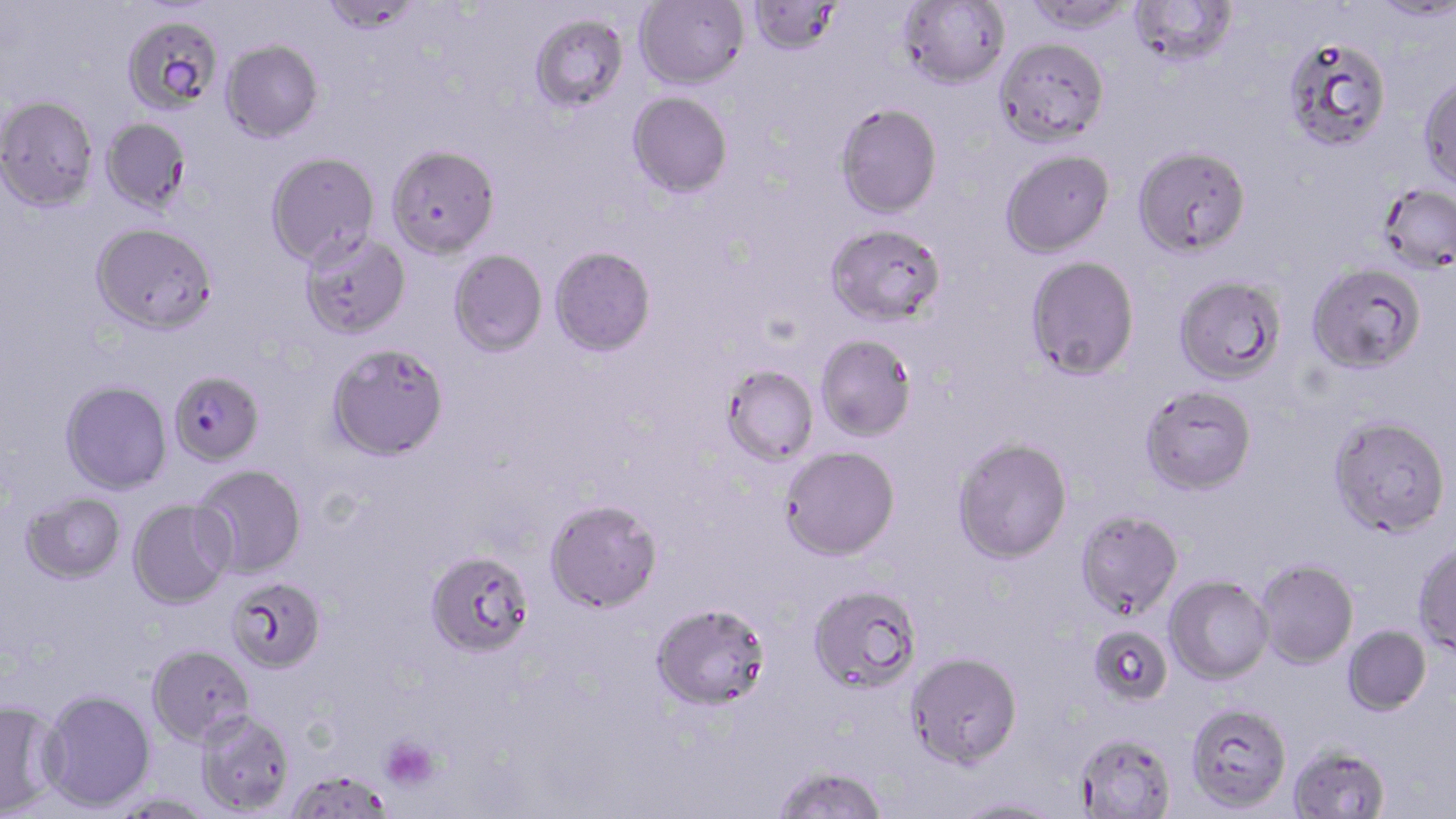
Approximate bounding boxes as (x1,y1)-(x2,y2) corner pairs in pixels. Platelet locations: (379,736)-(441,792). Plasmodium falciparum-infected red blood cell locations: (169,370)-(264,466). Uninfected red blood cell locations: (634,0)-(748,88), (746,0)-(845,56), (1021,0)-(1137,34), (1129,0)-(1238,67), (320,1)-(421,35), (898,1)-(1011,89), (1368,1)-(1456,22), (529,12)-(629,113), (122,14)-(224,116), (1281,35)-(1392,152), (995,36)-(1109,146), (221,39)-(324,142), (1418,73)-(1456,190), (627,91)-(733,198), (0,94)-(98,211), (835,102)-(942,218), (100,117)-(191,214), (387,144)-(501,259), (1132,144)-(1251,257), (1000,149)-(1115,258), (265,151)-(380,267), (1377,183)-(1456,273), (91,221)-(218,334), (825,222)-(946,328), (300,231)-(411,339), (550,246)-(657,357), (448,250)-(548,357), (1025,256)-(1140,380), (1307,262)-(1427,373), (1173,274)-(1287,384), (815,333)-(917,442), (327,343)-(450,461), (721,365)-(819,467), (60,381)-(172,494), (1139,384)-(1257,495), (1328,415)-(1451,538), (952,436)-(1073,564), (780,446)-(900,561), (193,465)-(307,578), (21,493)-(125,583), (128,498)-(234,609), (544,499)-(663,613), (1075,509)-(1183,620), (1413,540)-(1456,655), (425,550)-(535,659), (1255,559)-(1358,669), (1165,576)-(1273,684), (226,577)-(326,673), (807,583)-(922,693), (651,602)-(772,710), (1088,624)-(1173,706), (1342,625)-(1431,715), (147,644)-(254,746), (906,651)-(1023,768), (38,688)-(156,811), (0,699)-(63,817), (1186,701)-(1293,813), (195,709)-(295,815), (1075,732)-(1177,819), (1288,744)-(1392,819), (772,764)-(889,819), (286,768)-(394,818), (951,797)-(1064,818). Slide-level diagnosis: Plasmodium falciparum. May-Grünwald-Giemsa stain. Image is 1456×819 pixels. Thin blood smear. Light microscopy. 1000x magnification. One field of a larger specimen.